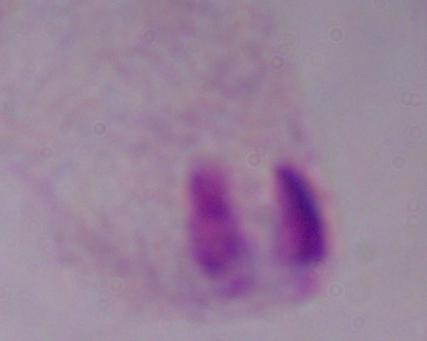

modality = photomicrograph
magnification = 1000x
identification = trichomonad